Classify this cell by malaria status.
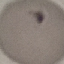

Uninfected.

stain = Giemsa
preparation = thin blood smear
image type = cell patch, automatically extracted from a larger field of view and resized to 64 × 64 pixels
capture = smartphone through the microscope eyepiece